Identify the parasite.
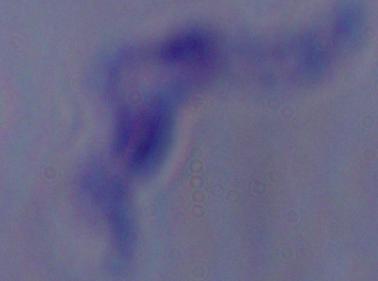
This is a trypanosome.

modality = micrograph
magnification = 1000x